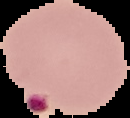
Summary:
  - Image size: 130×118 pixels
  - Result: Plasmodium parasites detected
  - Image type: segmented cell region on a black background
  - Preparation: thin blood film